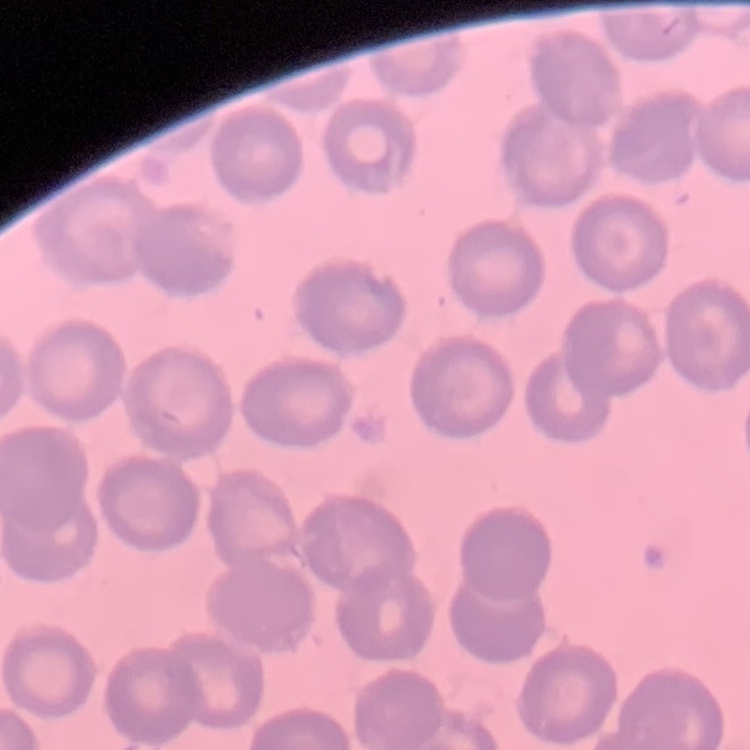

The red blood cells exhibit no rouleaux formation. Stained with either Field's or Giemsa. One tile cut from a larger photomicrograph. Thin blood film.